Outline each Plasmodium falciparum-infected red blood cell.
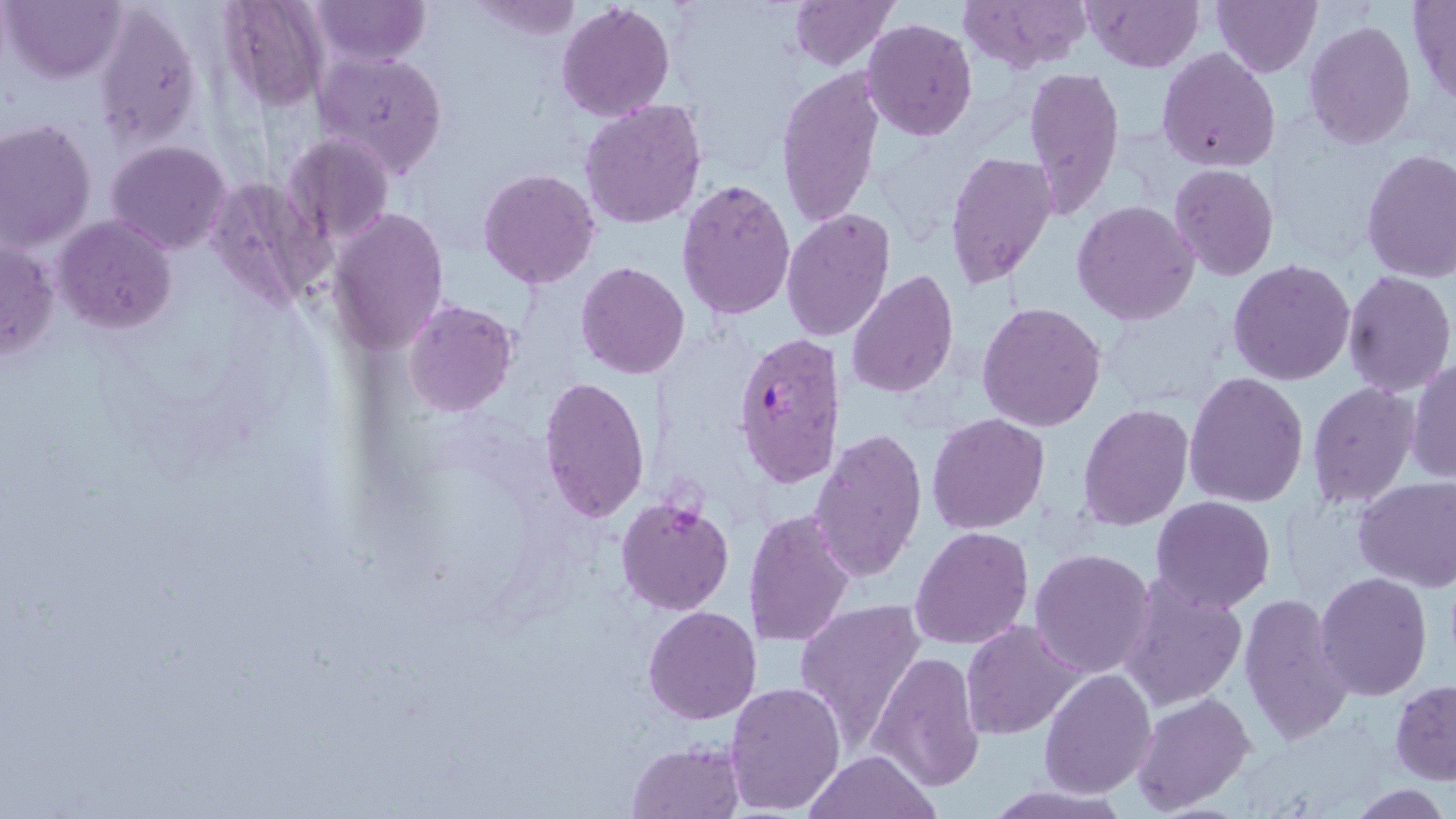
Approximate bounding boxes as named x1/y1/x2/y2 corners in pixels.
Plasmodium falciparum-infected red blood cells: (x1=733, y1=333, x2=844, y2=487).

Uninfected red blood cell locations: (x1=3, y1=0, x2=125, y2=84), (x1=311, y1=0, x2=429, y2=66), (x1=788, y1=0, x2=899, y2=72), (x1=959, y1=0, x2=1090, y2=73), (x1=1083, y1=0, x2=1201, y2=72), (x1=1211, y1=0, x2=1321, y2=77), (x1=465, y1=1, x2=584, y2=39), (x1=1407, y1=1, x2=1456, y2=105), (x1=216, y1=2, x2=331, y2=109), (x1=555, y1=2, x2=674, y2=121), (x1=95, y1=3, x2=204, y2=148), (x1=861, y1=18, x2=979, y2=140), (x1=1303, y1=21, x2=1417, y2=150), (x1=1157, y1=47, x2=1282, y2=171), (x1=312, y1=50, x2=448, y2=179), (x1=1022, y1=65, x2=1126, y2=218), (x1=774, y1=67, x2=886, y2=228), (x1=580, y1=98, x2=710, y2=230), (x1=1, y1=118, x2=96, y2=253), (x1=282, y1=133, x2=395, y2=249), (x1=105, y1=140, x2=233, y2=255), (x1=1360, y1=149, x2=1456, y2=282), (x1=945, y1=150, x2=1059, y2=290), (x1=1170, y1=163, x2=1280, y2=282), (x1=478, y1=168, x2=601, y2=290), (x1=205, y1=173, x2=328, y2=312), (x1=1083, y1=178, x2=1280, y2=299), (x1=675, y1=179, x2=798, y2=323), (x1=1072, y1=200, x2=1201, y2=325), (x1=327, y1=207, x2=450, y2=356), (x1=780, y1=207, x2=895, y2=342), (x1=54, y1=216, x2=177, y2=334), (x1=0, y1=238, x2=58, y2=362), (x1=1228, y1=258, x2=1357, y2=387), (x1=574, y1=261, x2=691, y2=380), (x1=846, y1=270, x2=959, y2=397), (x1=1341, y1=271, x2=1455, y2=396), (x1=403, y1=300, x2=518, y2=418), (x1=977, y1=301, x2=1108, y2=432), (x1=1407, y1=358, x2=1455, y2=485), (x1=1184, y1=370, x2=1309, y2=507), (x1=538, y1=376, x2=651, y2=524), (x1=1307, y1=383, x2=1420, y2=508), (x1=1078, y1=405, x2=1194, y2=532), (x1=927, y1=411, x2=1049, y2=534), (x1=809, y1=430, x2=926, y2=584), (x1=1355, y1=476, x2=1456, y2=592), (x1=615, y1=496, x2=736, y2=617), (x1=1149, y1=496, x2=1276, y2=613), (x1=742, y1=510, x2=855, y2=650), (x1=911, y1=526, x2=1033, y2=649), (x1=1029, y1=549, x2=1156, y2=678), (x1=1315, y1=572, x2=1433, y2=700), (x1=1118, y1=575, x2=1248, y2=714), (x1=1239, y1=592, x2=1353, y2=745), (x1=794, y1=599, x2=927, y2=747), (x1=643, y1=606, x2=762, y2=726), (x1=960, y1=620, x2=1083, y2=739), (x1=870, y1=652, x2=984, y2=791), (x1=1039, y1=669, x2=1158, y2=796), (x1=1390, y1=680, x2=1456, y2=784), (x1=724, y1=681, x2=848, y2=815), (x1=1130, y1=690, x2=1257, y2=813), (x1=627, y1=740, x2=743, y2=818), (x1=803, y1=751, x2=939, y2=819), (x1=977, y1=783, x2=1134, y2=817), (x1=1347, y1=784, x2=1450, y2=817). Slide-level diagnosis: Plasmodium falciparum. Single field of view. May-Grünwald-Giemsa stain. Captured at 1000x magnification. Thin blood film. Image is 1456×819 pixels. Optical microscopy.